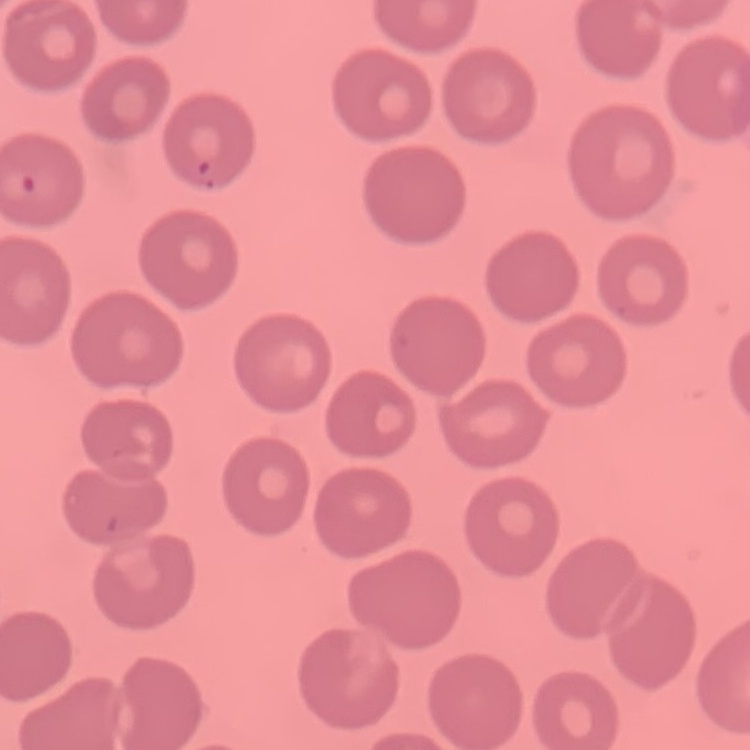
Summary:
  - Erythrocyte morphology: no rouleaux formation
  - Stain: Field's or Giemsa
  - Preparation: thin peripheral smear
  - Image type: one tile cut from a larger photomicrograph